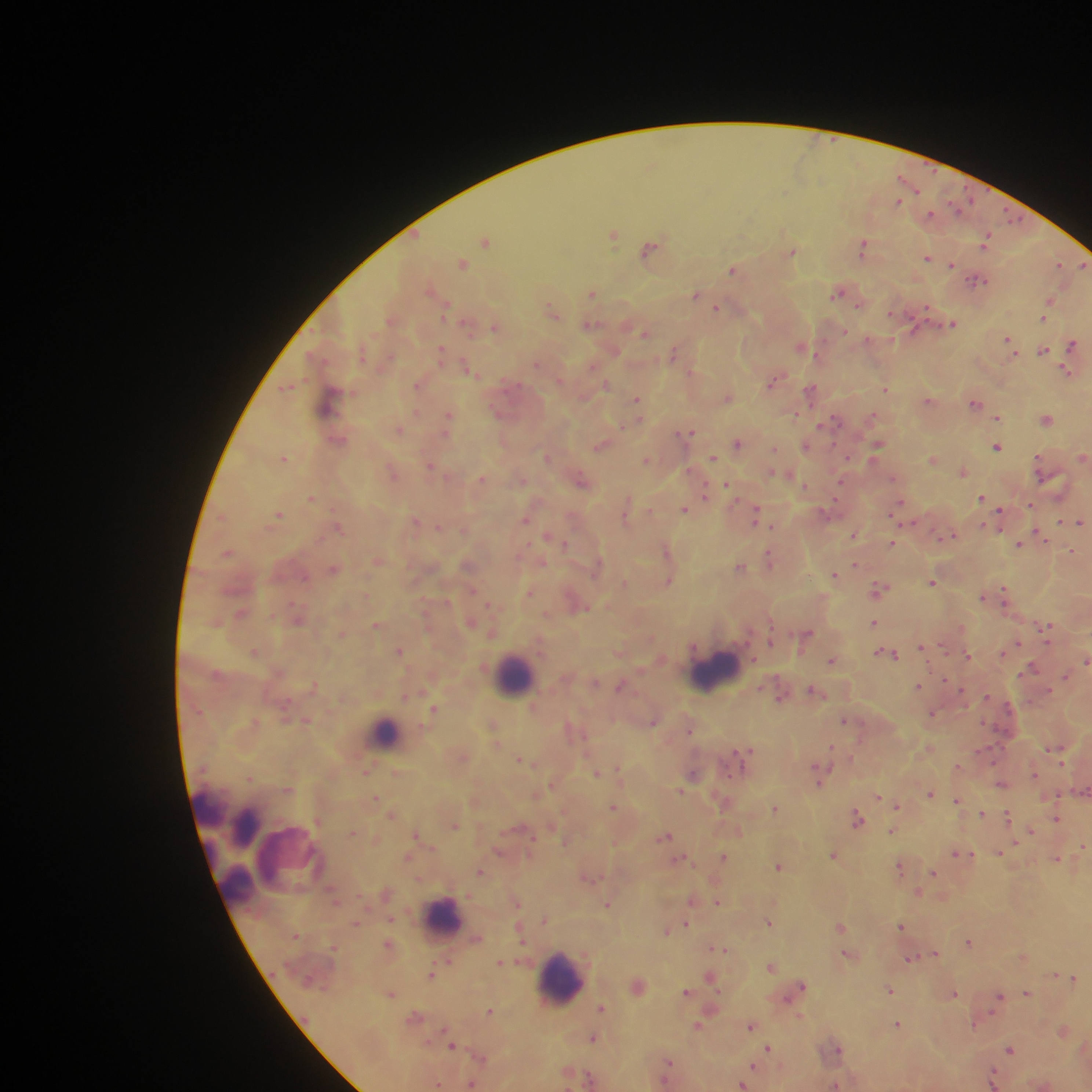
capture = mobile-phone photograph through a microscope
leukocyte locations = approximate centers as (x, y) in pixels: (715, 672), (515, 675), (386, 732), (207, 808), (244, 828), (290, 859), (239, 887), (442, 919), (562, 980)
image size = 1092×1092 pixels
field of view = single
preparation = thick blood film
Plasmodium parasite locations = approximate centers as (x, y) in pixels: (909, 183), (898, 201), (930, 215), (614, 234), (486, 241), (985, 242), (864, 247), (652, 248), (792, 252), (927, 257), (1059, 263), (463, 264), (952, 264), (1084, 265), (734, 269), (976, 280), (841, 291), (592, 292), (697, 296), (1050, 301), (716, 307), (1047, 307), (553, 311), (1044, 316), (954, 323), (469, 325), (496, 325), (590, 326), (645, 332), (1008, 339), (870, 340), (1073, 343), (803, 347), (1043, 349), (614, 350), (675, 351), (442, 352), (538, 363), (470, 368), (1067, 371), (692, 373), (776, 379), (419, 383), (607, 384), (288, 387), (886, 388), (811, 390), (728, 396), (330, 400), (637, 400), (930, 400), (975, 403), (796, 412), (449, 416), (873, 416), (998, 417), (1048, 420), (833, 421), (400, 429), (687, 432), (337, 439), (738, 442), (877, 444), (602, 445), (997, 445), (806, 446), (774, 449), (547, 456), (284, 457), (712, 457), (1083, 457), (933, 458), (647, 459), (1040, 463), (431, 466), (964, 471), (394, 472), (774, 473), (786, 473), (483, 479), (894, 479), (582, 480), (728, 484), (805, 486), (705, 496), (312, 498), (982, 498), (899, 505), (1030, 505), (684, 508), (626, 509), (278, 514), (757, 514), (1000, 515), (526, 518), (1063, 521), (416, 522), (1080, 522), (339, 527), (855, 534), (950, 537), (1042, 537), (553, 539), (892, 543), (1019, 543), (667, 550), (1072, 552), (229, 553), (770, 558), (379, 560), (855, 564), (468, 565), (597, 565), (740, 566), (334, 569), (835, 575), (668, 581), (932, 582), (624, 583), (879, 589), (530, 593), (1004, 595), (983, 596), (577, 602), (241, 613), (298, 617), (471, 622), (874, 623), (377, 625), (1045, 626), (341, 633), (493, 633), (807, 633), (771, 640), (923, 647), (1009, 647), (399, 650), (620, 650), (254, 651), (1005, 651), (888, 652), (967, 656), (832, 660), (1086, 661), (1032, 668), (1066, 676), (315, 685), (918, 685), (622, 686), (816, 691), (781, 696), (435, 708), (932, 714), (307, 719), (845, 720), (653, 721), (255, 722), (493, 725), (689, 727), (929, 748), (1055, 749), (746, 752), (463, 756), (525, 759), (958, 767), (366, 771), (819, 771), (398, 773), (596, 773), (620, 773), (694, 773), (1034, 773), (250, 777), (1002, 784), (553, 785), (287, 788), (680, 791), (1081, 791), (930, 793), (879, 796), (375, 798), (957, 800), (724, 801), (475, 802), (897, 804), (613, 806), (775, 808), (982, 814), (392, 815), (858, 817), (1007, 817), (1057, 818), (455, 825), (738, 830), (1031, 830), (892, 831), (352, 832), (417, 834), (666, 835), (565, 840), (1084, 846), (1000, 851), (500, 852), (961, 854), (834, 855), (408, 857), (723, 857), (1057, 858), (680, 859), (779, 865), (901, 867), (481, 871), (933, 873), (588, 877), (918, 892), (692, 900), (717, 901), (516, 902), (608, 903), (391, 918), (545, 919), (769, 922), (356, 923), (686, 924), (841, 925), (901, 926), (666, 930), (968, 942), (388, 945), (335, 946), (719, 949), (935, 953), (849, 954), (1024, 957), (912, 958), (448, 961), (501, 962), (771, 965), (432, 974), (1056, 974), (710, 975), (1073, 978), (638, 984), (801, 985), (890, 989), (687, 992), (1026, 992), (392, 993), (954, 993), (1001, 996), (602, 1007), (712, 1008), (490, 1010), (415, 1017), (799, 1017), (976, 1023), (898, 1024), (697, 1025), (751, 1025), (1064, 1030), (593, 1037), (452, 1045), (769, 1047), (838, 1047), (1011, 1048), (481, 1056), (669, 1062), (754, 1066), (667, 1072), (994, 1077), (590, 1078), (472, 1083), (438, 1084), (742, 1084), (835, 1084)
country = Ghana